Classify this cell by malaria status.
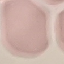

It is uninfected.

Summary:
  - Preparation: thin blood film
  - Stain: Giemsa
  - Capture: smartphone camera at the microscope eyepiece
  - Image type: automatically extracted cell patch, resized to 64 × 64 pixels